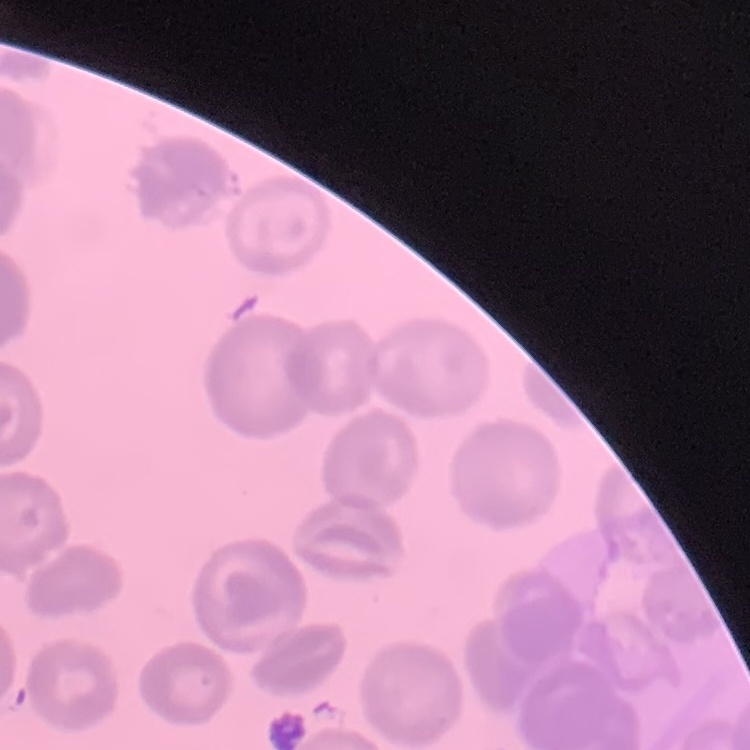

The erythrocytes show no rouleaux formation. One tile cut from a larger photomicrograph. Thin blood film. Field's or Giemsa stain.